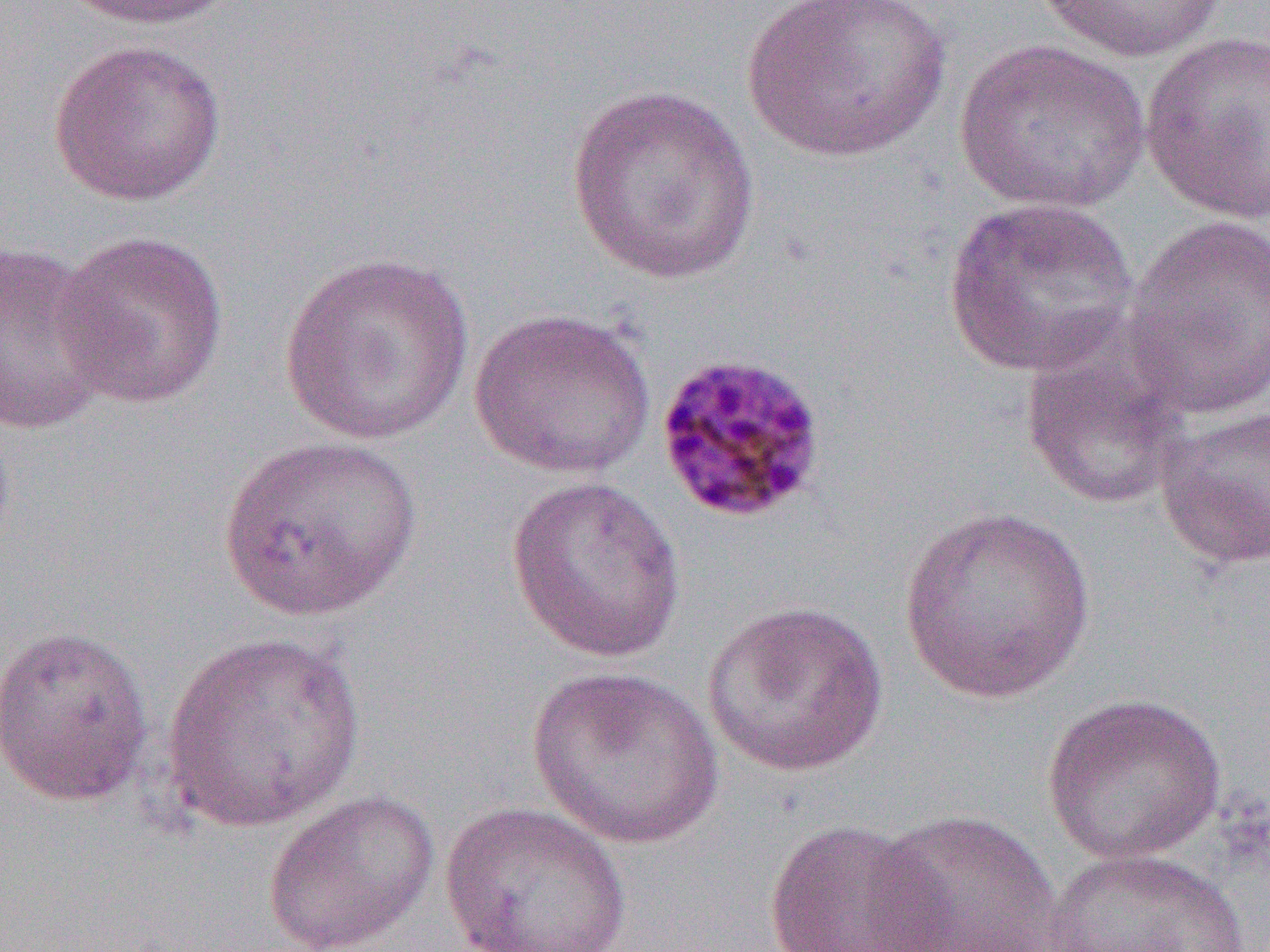 Approximate bounding boxes as (x1, y1, x2, y2) in pixels. Uninfected red blood cell locations: (61, 0, 236, 31), (739, 0, 953, 164), (1033, 0, 1226, 64), (1139, 31, 1270, 224), (48, 38, 227, 207), (953, 39, 1150, 216), (564, 83, 761, 285), (941, 196, 1139, 378), (1122, 214, 1270, 422), (51, 228, 231, 410), (1, 240, 115, 436), (278, 251, 475, 447), (469, 306, 656, 479), (1018, 328, 1192, 512), (1153, 404, 1270, 570), (216, 435, 423, 622), (505, 475, 686, 664), (897, 507, 1097, 704), (701, 599, 890, 778), (0, 623, 155, 808), (161, 631, 367, 833), (526, 664, 723, 849), (1041, 691, 1228, 866), (262, 789, 440, 952), (439, 801, 633, 952), (867, 809, 1062, 952), (762, 819, 946, 952), (1037, 846, 1263, 952). Plasmodium malariae-infected red blood cell locations: (653, 351, 829, 525). Slide-level diagnosis: Plasmodium malariae. Thin blood film. Optical microscopy. Image is 1270×952 pixels. One field of a larger specimen. 1000x magnification.